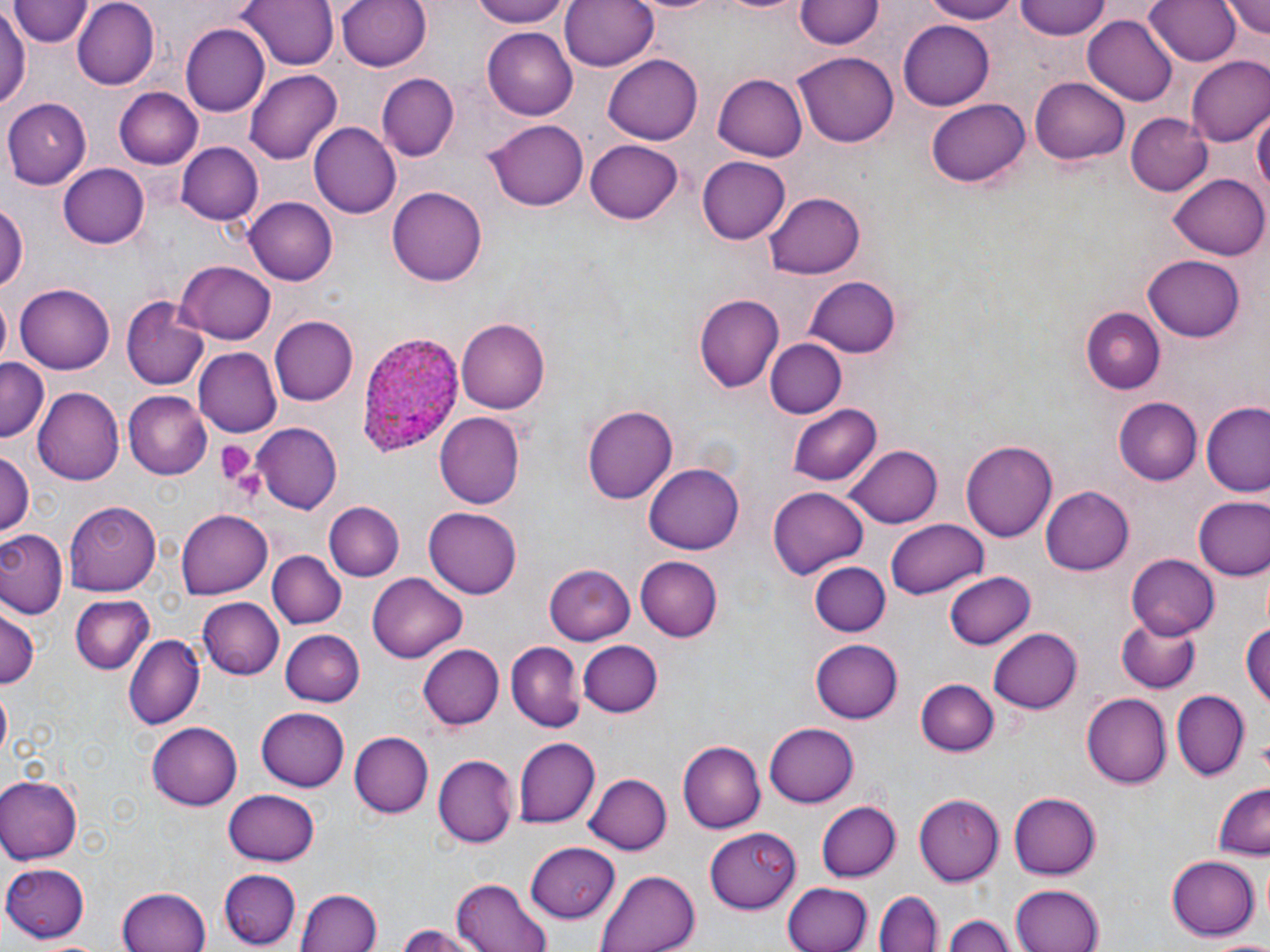

Summary:
  - Coordinate format: approximate bounding boxes as named x1/y1/x2/y2 corners in pixels
  - Plasmodium ovale-infected red blood cell locations: (x1=355, y1=332, x2=465, y2=456)
  - Platelet locations: (x1=212, y1=439, x2=262, y2=491)
  - Uninfected red blood cell locations: (x1=73, y1=0, x2=159, y2=89), (x1=236, y1=0, x2=340, y2=71), (x1=337, y1=0, x2=433, y2=73), (x1=467, y1=0, x2=574, y2=27), (x1=560, y1=0, x2=659, y2=73), (x1=920, y1=0, x2=1018, y2=23), (x1=1015, y1=0, x2=1114, y2=39), (x1=1144, y1=0, x2=1241, y2=67), (x1=1222, y1=0, x2=1270, y2=42), (x1=11, y1=1, x2=93, y2=48), (x1=797, y1=1, x2=883, y2=49), (x1=1191, y1=1, x2=1270, y2=53), (x1=0, y1=6, x2=29, y2=113), (x1=1083, y1=16, x2=1179, y2=105), (x1=898, y1=17, x2=994, y2=107), (x1=182, y1=24, x2=268, y2=114), (x1=483, y1=27, x2=579, y2=119), (x1=794, y1=52, x2=899, y2=146), (x1=1188, y1=55, x2=1270, y2=147), (x1=604, y1=57, x2=703, y2=144), (x1=245, y1=70, x2=341, y2=163), (x1=713, y1=72, x2=809, y2=160), (x1=378, y1=74, x2=457, y2=159), (x1=1029, y1=76, x2=1129, y2=164), (x1=112, y1=87, x2=203, y2=167), (x1=928, y1=96, x2=1029, y2=185), (x1=3, y1=98, x2=91, y2=187), (x1=1251, y1=106, x2=1268, y2=205), (x1=1125, y1=111, x2=1212, y2=196), (x1=488, y1=117, x2=589, y2=210), (x1=309, y1=122, x2=401, y2=218), (x1=585, y1=138, x2=683, y2=224), (x1=176, y1=140, x2=262, y2=226), (x1=696, y1=156, x2=789, y2=245), (x1=58, y1=162, x2=148, y2=246), (x1=1170, y1=173, x2=1269, y2=259), (x1=388, y1=183, x2=487, y2=283), (x1=766, y1=192, x2=865, y2=280), (x1=245, y1=196, x2=337, y2=285), (x1=0, y1=199, x2=26, y2=299), (x1=1144, y1=254, x2=1245, y2=341), (x1=175, y1=261, x2=276, y2=344), (x1=805, y1=276, x2=901, y2=356), (x1=16, y1=283, x2=114, y2=375), (x1=695, y1=295, x2=783, y2=393), (x1=122, y1=301, x2=208, y2=390), (x1=1080, y1=304, x2=1167, y2=395), (x1=269, y1=316, x2=358, y2=407), (x1=456, y1=318, x2=550, y2=414), (x1=764, y1=339, x2=845, y2=418), (x1=194, y1=348, x2=282, y2=436), (x1=0, y1=359, x2=50, y2=438), (x1=36, y1=386, x2=125, y2=486), (x1=122, y1=392, x2=211, y2=479), (x1=1114, y1=398, x2=1202, y2=484), (x1=788, y1=403, x2=880, y2=484), (x1=582, y1=405, x2=678, y2=506), (x1=1202, y1=405, x2=1270, y2=496), (x1=435, y1=412, x2=526, y2=507), (x1=252, y1=423, x2=341, y2=512), (x1=961, y1=438, x2=1056, y2=539), (x1=847, y1=445, x2=942, y2=528), (x1=1, y1=451, x2=34, y2=537), (x1=645, y1=461, x2=743, y2=553), (x1=1040, y1=486, x2=1133, y2=576), (x1=768, y1=488, x2=869, y2=579), (x1=1192, y1=495, x2=1270, y2=582), (x1=66, y1=500, x2=158, y2=596), (x1=325, y1=502, x2=402, y2=580), (x1=314, y1=504, x2=481, y2=586), (x1=424, y1=509, x2=522, y2=598), (x1=177, y1=510, x2=273, y2=597), (x1=886, y1=520, x2=989, y2=600), (x1=0, y1=529, x2=67, y2=617), (x1=269, y1=551, x2=345, y2=629), (x1=1126, y1=552, x2=1218, y2=638), (x1=635, y1=555, x2=723, y2=642), (x1=808, y1=559, x2=890, y2=636), (x1=547, y1=564, x2=637, y2=643), (x1=944, y1=570, x2=1037, y2=649), (x1=366, y1=573, x2=469, y2=662), (x1=70, y1=595, x2=156, y2=675), (x1=199, y1=599, x2=284, y2=679), (x1=0, y1=607, x2=39, y2=692), (x1=1242, y1=613, x2=1269, y2=718), (x1=1114, y1=615, x2=1202, y2=693), (x1=280, y1=629, x2=364, y2=706), (x1=990, y1=629, x2=1083, y2=713), (x1=125, y1=634, x2=203, y2=729), (x1=809, y1=638, x2=903, y2=723), (x1=578, y1=640, x2=662, y2=718), (x1=507, y1=641, x2=583, y2=731), (x1=419, y1=643, x2=503, y2=731), (x1=917, y1=679, x2=998, y2=757), (x1=1172, y1=690, x2=1249, y2=781), (x1=0, y1=692, x2=10, y2=755), (x1=1084, y1=693, x2=1172, y2=787), (x1=256, y1=708, x2=350, y2=792), (x1=147, y1=722, x2=243, y2=810), (x1=764, y1=724, x2=860, y2=807), (x1=349, y1=732, x2=432, y2=817), (x1=514, y1=737, x2=599, y2=829), (x1=678, y1=741, x2=764, y2=834), (x1=436, y1=753, x2=520, y2=848), (x1=583, y1=773, x2=672, y2=855), (x1=0, y1=776, x2=80, y2=864), (x1=1211, y1=782, x2=1269, y2=858), (x1=223, y1=790, x2=321, y2=867), (x1=1008, y1=791, x2=1100, y2=880), (x1=914, y1=792, x2=1003, y2=885), (x1=818, y1=800, x2=900, y2=882), (x1=705, y1=826, x2=801, y2=912), (x1=525, y1=842, x2=621, y2=922), (x1=1167, y1=854, x2=1260, y2=941), (x1=2, y1=862, x2=91, y2=940), (x1=219, y1=869, x2=300, y2=948), (x1=596, y1=869, x2=700, y2=952), (x1=451, y1=877, x2=552, y2=952), (x1=782, y1=882, x2=870, y2=952), (x1=1009, y1=885, x2=1104, y2=952), (x1=118, y1=889, x2=211, y2=952), (x1=298, y1=890, x2=380, y2=952), (x1=876, y1=891, x2=943, y2=952), (x1=944, y1=912, x2=1015, y2=952), (x1=392, y1=925, x2=486, y2=952), (x1=1213, y1=937, x2=1270, y2=950)
  - Slide-level diagnosis: Plasmodium ovale
  - Modality: optical microscopy
  - Magnification: 1000x
  - Preparation: thin blood smear
  - Image size: 1270×952 pixels
  - Field of view: one of a larger specimen
  - Stain: May-Grünwald-Giemsa